Locate and identify every blood parasite.
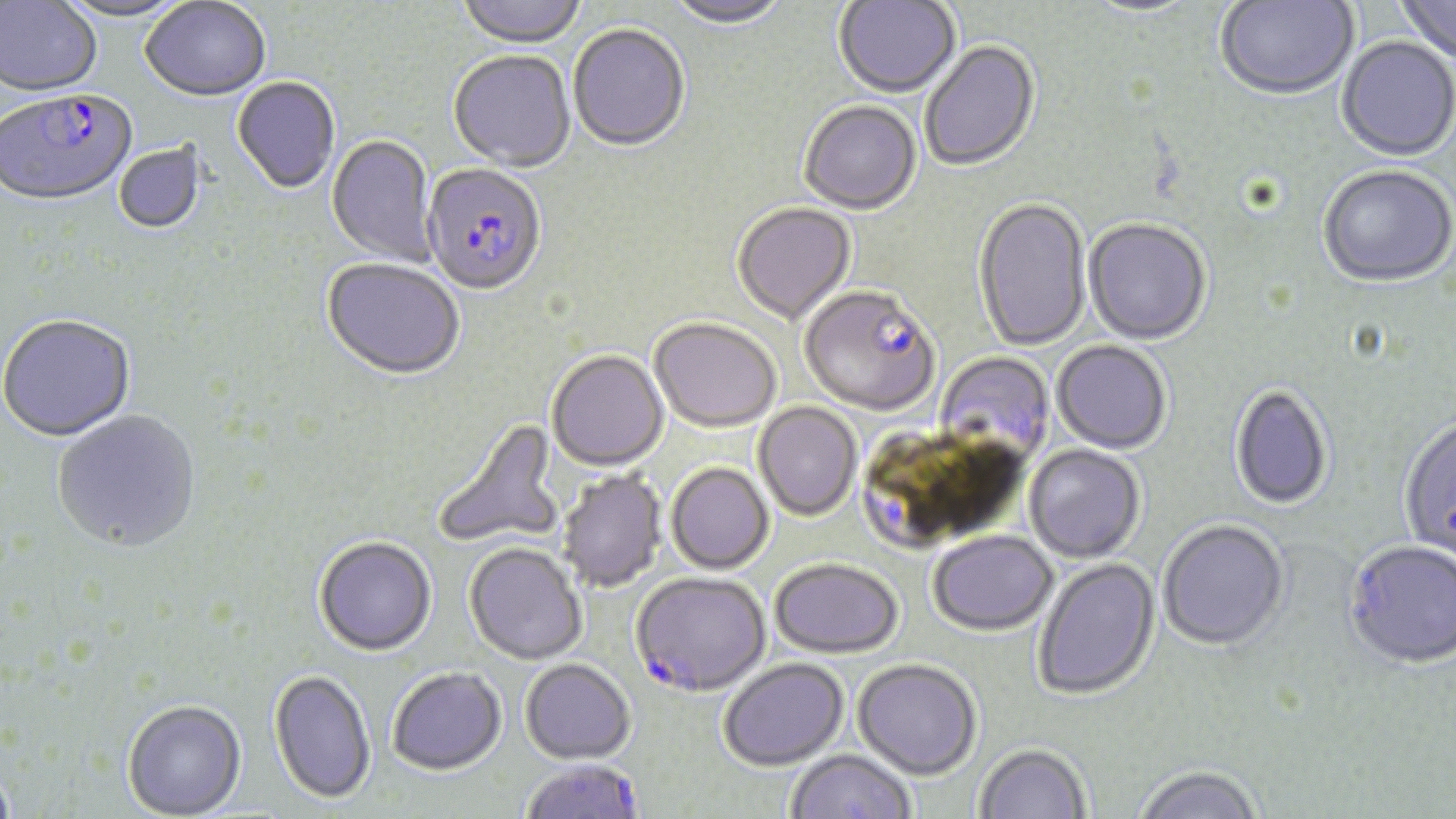

Approximate bounding boxes as named x1/y1/x2/y2 corners in pixels.
Plasmodium falciparum-infected red blood cells: (x1=1, y1=92, x2=138, y2=210), (x1=420, y1=166, x2=546, y2=298), (x1=800, y1=289, x2=940, y2=418), (x1=630, y1=575, x2=770, y2=699), (x1=521, y1=761, x2=644, y2=819).
No Plasmodium ovale, Plasmodium malariae, Plasmodium vivax, Babesia divergens, or Trypanosoma brucei observed.

Uninfected red blood cell locations: (x1=52, y1=0, x2=193, y2=24), (x1=455, y1=0, x2=587, y2=51), (x1=663, y1=0, x2=793, y2=31), (x1=834, y1=0, x2=961, y2=99), (x1=1215, y1=0, x2=1359, y2=102), (x1=1396, y1=0, x2=1456, y2=67), (x1=141, y1=1, x2=271, y2=104), (x1=1079, y1=1, x2=1206, y2=19), (x1=0, y1=2, x2=102, y2=98), (x1=568, y1=26, x2=690, y2=155), (x1=1336, y1=38, x2=1456, y2=164), (x1=920, y1=42, x2=1041, y2=173), (x1=448, y1=53, x2=576, y2=174), (x1=232, y1=78, x2=341, y2=196), (x1=799, y1=102, x2=922, y2=217), (x1=327, y1=135, x2=438, y2=266), (x1=114, y1=142, x2=207, y2=236), (x1=1318, y1=167, x2=1456, y2=290), (x1=972, y1=199, x2=1091, y2=354), (x1=732, y1=204, x2=857, y2=326), (x1=1083, y1=219, x2=1212, y2=346), (x1=321, y1=260, x2=464, y2=383), (x1=0, y1=316, x2=137, y2=443), (x1=649, y1=320, x2=782, y2=435), (x1=1051, y1=342, x2=1171, y2=455), (x1=546, y1=352, x2=669, y2=473), (x1=935, y1=352, x2=1056, y2=462), (x1=1229, y1=386, x2=1332, y2=511), (x1=753, y1=402, x2=862, y2=523), (x1=52, y1=410, x2=201, y2=555), (x1=432, y1=417, x2=563, y2=548), (x1=1398, y1=417, x2=1456, y2=567), (x1=1024, y1=445, x2=1145, y2=564), (x1=666, y1=464, x2=773, y2=576), (x1=558, y1=471, x2=667, y2=593), (x1=1157, y1=521, x2=1289, y2=653), (x1=928, y1=532, x2=1057, y2=638), (x1=313, y1=538, x2=437, y2=658), (x1=1344, y1=542, x2=1456, y2=673), (x1=464, y1=544, x2=587, y2=667), (x1=1034, y1=558, x2=1161, y2=702), (x1=770, y1=560, x2=902, y2=661), (x1=719, y1=660, x2=849, y2=773), (x1=520, y1=661, x2=636, y2=766), (x1=853, y1=661, x2=981, y2=782), (x1=387, y1=669, x2=507, y2=778), (x1=268, y1=671, x2=376, y2=806), (x1=122, y1=701, x2=247, y2=819), (x1=975, y1=745, x2=1091, y2=819), (x1=786, y1=751, x2=915, y2=818), (x1=0, y1=765, x2=18, y2=819), (x1=1132, y1=767, x2=1264, y2=819). Slide-level diagnosis: Plasmodium falciparum. Captured at 1000x magnification. Single field of view. Image is 1456×819 pixels. Optical microscopy. Thin blood smear. May-Grünwald-Giemsa stain.